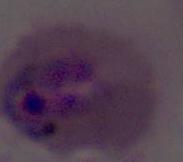
Summary:
  - Modality: photomicrograph
  - Identification: Plasmodium
  - Magnification: 400x or 1000x